Name the blood parasite species.
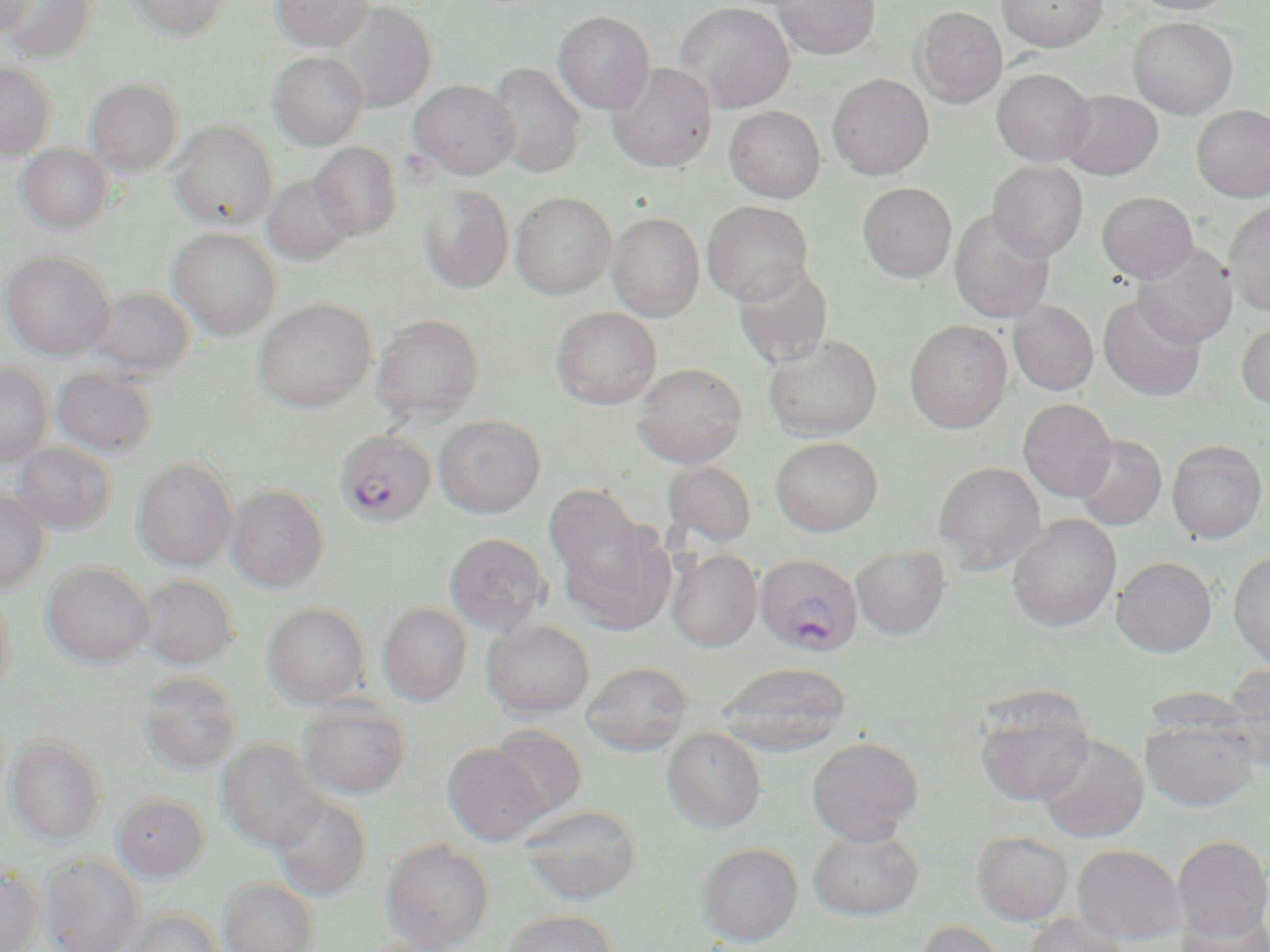
Plasmodium falciparum.

preparation = thin blood smear
modality = light microscopy
stain = May-Grünwald-Giemsa
image size = 1270×952 pixels
Plasmodium falciparum-infected red blood cell locations = approximate bounding boxes as [x1, y1, x2, y2] in pixels: [333, 429, 437, 528], [755, 553, 863, 657]
field of view = one of a larger specimen
uninfected red blood cell locations = approximate bounding boxes as [x1, y1, x2, y2] in pixels: [1, 0, 96, 63], [1, 0, 36, 35], [124, 0, 228, 41], [270, 0, 374, 51], [773, 0, 880, 60], [997, 0, 1107, 51], [1127, 0, 1237, 14], [674, 1, 795, 112], [333, 2, 436, 112], [913, 6, 1008, 107], [553, 11, 654, 114], [1128, 17, 1239, 118], [267, 52, 368, 150], [607, 61, 718, 171], [0, 62, 56, 159], [487, 62, 587, 178], [992, 68, 1094, 165], [827, 73, 934, 179], [84, 78, 184, 176], [408, 79, 520, 180], [1059, 90, 1164, 180], [1192, 104, 1270, 202], [724, 105, 826, 203], [168, 121, 278, 231], [309, 142, 401, 240], [16, 144, 113, 234], [988, 161, 1088, 261], [261, 174, 356, 265], [858, 182, 957, 282], [418, 184, 514, 293], [1097, 191, 1198, 283], [510, 192, 617, 299], [702, 201, 813, 305], [1224, 201, 1270, 317], [949, 210, 1055, 324], [607, 212, 705, 322], [167, 227, 281, 340], [1132, 243, 1238, 348], [0, 250, 115, 360], [732, 263, 834, 370], [83, 286, 195, 381], [1098, 294, 1206, 402], [253, 298, 376, 412], [1009, 300, 1098, 396], [551, 307, 662, 409], [371, 313, 486, 423], [904, 319, 1013, 434], [1236, 320, 1270, 410], [763, 333, 882, 441], [632, 362, 748, 468], [0, 364, 52, 466], [51, 367, 157, 457], [1018, 398, 1118, 502], [433, 415, 546, 518], [1073, 435, 1167, 531], [770, 436, 883, 536], [1167, 439, 1267, 543], [11, 441, 116, 535], [132, 457, 238, 571], [662, 461, 757, 547], [933, 461, 1046, 573], [226, 484, 329, 592], [545, 484, 647, 589], [0, 489, 49, 592], [1008, 513, 1121, 632], [557, 519, 677, 636], [444, 532, 551, 636], [851, 545, 949, 640], [666, 548, 762, 652], [1228, 550, 1270, 669], [1112, 555, 1217, 657], [41, 562, 154, 668], [134, 574, 239, 669], [0, 586, 14, 702], [262, 602, 369, 708], [377, 603, 472, 706], [481, 619, 595, 718], [581, 660, 694, 756], [716, 661, 853, 755], [1219, 667, 1270, 767], [134, 671, 243, 777], [973, 693, 1095, 806], [297, 698, 411, 800], [1141, 718, 1259, 812], [488, 724, 587, 819], [662, 726, 766, 833], [5, 735, 107, 845], [1037, 735, 1148, 842], [806, 736, 924, 845], [216, 739, 331, 853], [443, 743, 550, 846], [111, 791, 209, 881], [271, 795, 372, 901], [518, 804, 643, 905], [808, 828, 923, 921], [972, 831, 1074, 925], [1172, 835, 1270, 942], [381, 839, 495, 952], [695, 842, 803, 946], [1073, 844, 1186, 944], [39, 853, 144, 952], [0, 866, 45, 952], [218, 879, 319, 952], [123, 907, 225, 952], [502, 909, 619, 952], [1174, 912, 1269, 952], [1023, 913, 1130, 952], [912, 919, 1010, 952]
magnification = 1000x